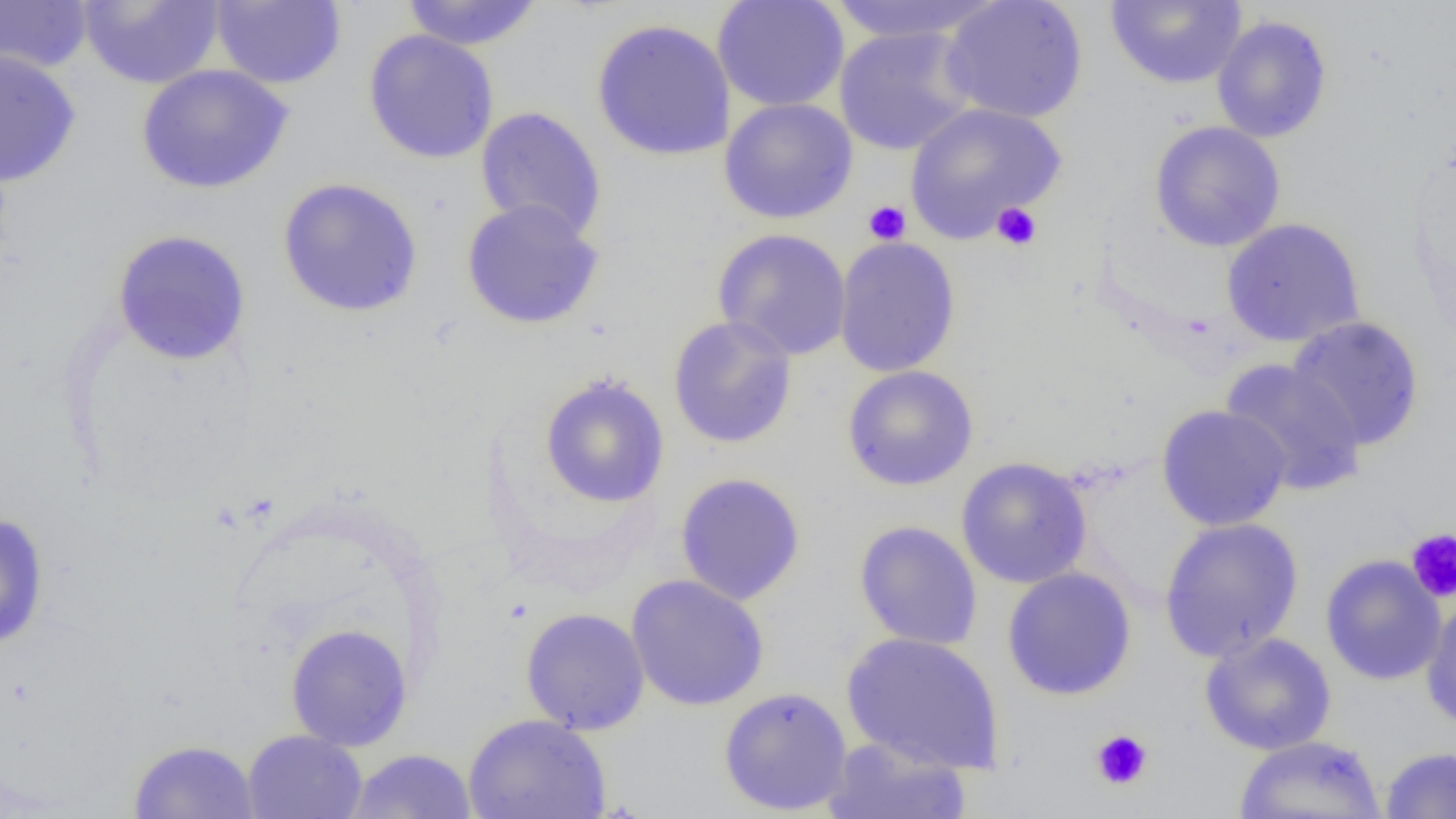

Summary:
  - Coordinate format: approximate bounding boxes as (x1, y1, x2, y2) in pixels
  - Uninfected red blood cell locations: (78, 0, 225, 89), (401, 0, 544, 51), (712, 0, 849, 112), (822, 0, 1005, 45), (939, 0, 1089, 124), (1106, 0, 1247, 89), (0, 1, 94, 74), (211, 1, 346, 89), (1212, 14, 1332, 143), (591, 18, 736, 162), (834, 26, 978, 156), (363, 30, 499, 164), (0, 49, 82, 187), (136, 64, 294, 194), (718, 97, 858, 224), (904, 102, 1066, 241), (474, 107, 608, 243), (1149, 121, 1286, 252), (276, 177, 424, 318), (461, 198, 605, 330), (1221, 217, 1366, 348), (712, 228, 852, 360), (111, 229, 252, 366), (833, 236, 962, 378), (667, 315, 798, 449), (1286, 315, 1425, 451), (1219, 358, 1367, 496), (841, 364, 979, 491), (539, 373, 670, 509), (1156, 404, 1292, 531), (955, 456, 1093, 589), (674, 472, 806, 606), (0, 512, 50, 650), (1159, 517, 1304, 662), (854, 520, 983, 651), (1320, 554, 1446, 686), (1001, 567, 1137, 701), (626, 574, 769, 712), (1421, 593, 1456, 732), (520, 607, 650, 734), (285, 623, 414, 750), (840, 631, 1005, 775), (1199, 631, 1337, 755), (718, 686, 853, 816), (462, 713, 612, 819), (242, 730, 368, 819), (1234, 734, 1387, 818), (822, 736, 972, 818), (128, 739, 261, 819), (1380, 746, 1456, 818), (347, 748, 477, 818)
  - Platelet locations: (863, 200, 911, 245), (991, 202, 1041, 251), (1406, 529, 1456, 603), (1090, 729, 1153, 791)
  - Slide-level diagnosis: negative for blood parasites
  - Image size: 1456×819 pixels
  - Modality: light microscopy
  - Preparation: thin blood film
  - Field of view: one of a larger specimen
  - Magnification: 1000x